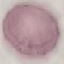

Result: no malaria parasites seen. Photographed with a smartphone camera at the microscope eyepiece. Thin blood film. Automatically extracted cell patch, resized to 64 × 64 pixels. Giemsa stain.